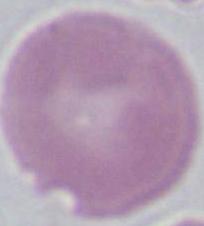
identification = erythrocyte
magnification = 1000x
modality = micrograph